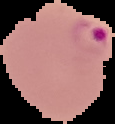

Image is 115×124 pixels. From a thin blood film. Result: Plasmodium parasites detected. Segmented cell region on a black background.